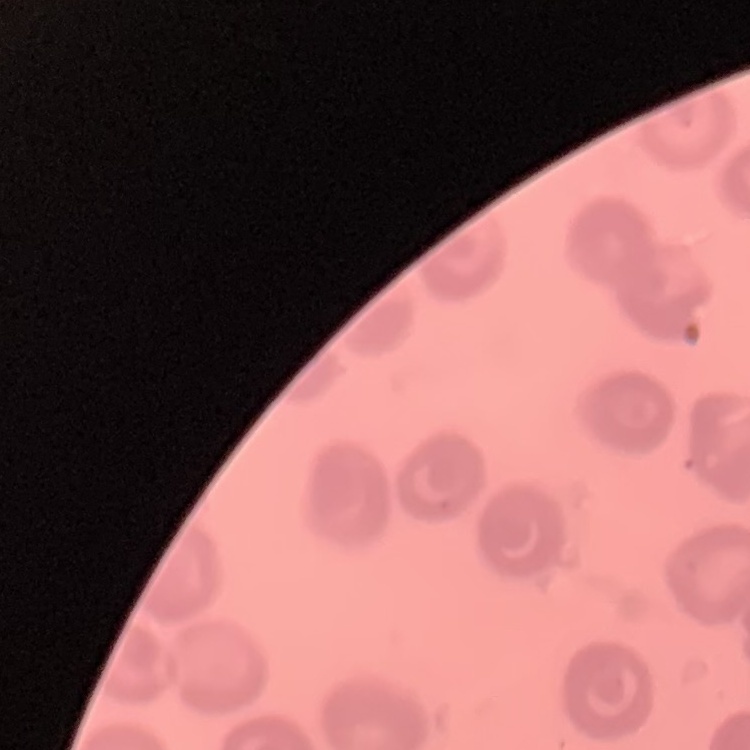 The red blood cells show no rouleaux formation. One tile cut from a larger photomicrograph. Thin blood smear. Stained with either Field's or Giemsa.